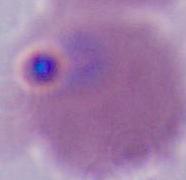
{
  "magnification": "400x or 1000x",
  "identification": "Plasmodium",
  "modality": "photomicrograph"
}